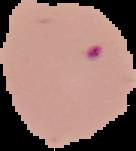

Segmented cell region on a black background. From a thin blood film. Image is 136×151 pixels. Result: malaria parasites identified.